Locate and identify every blood parasite.
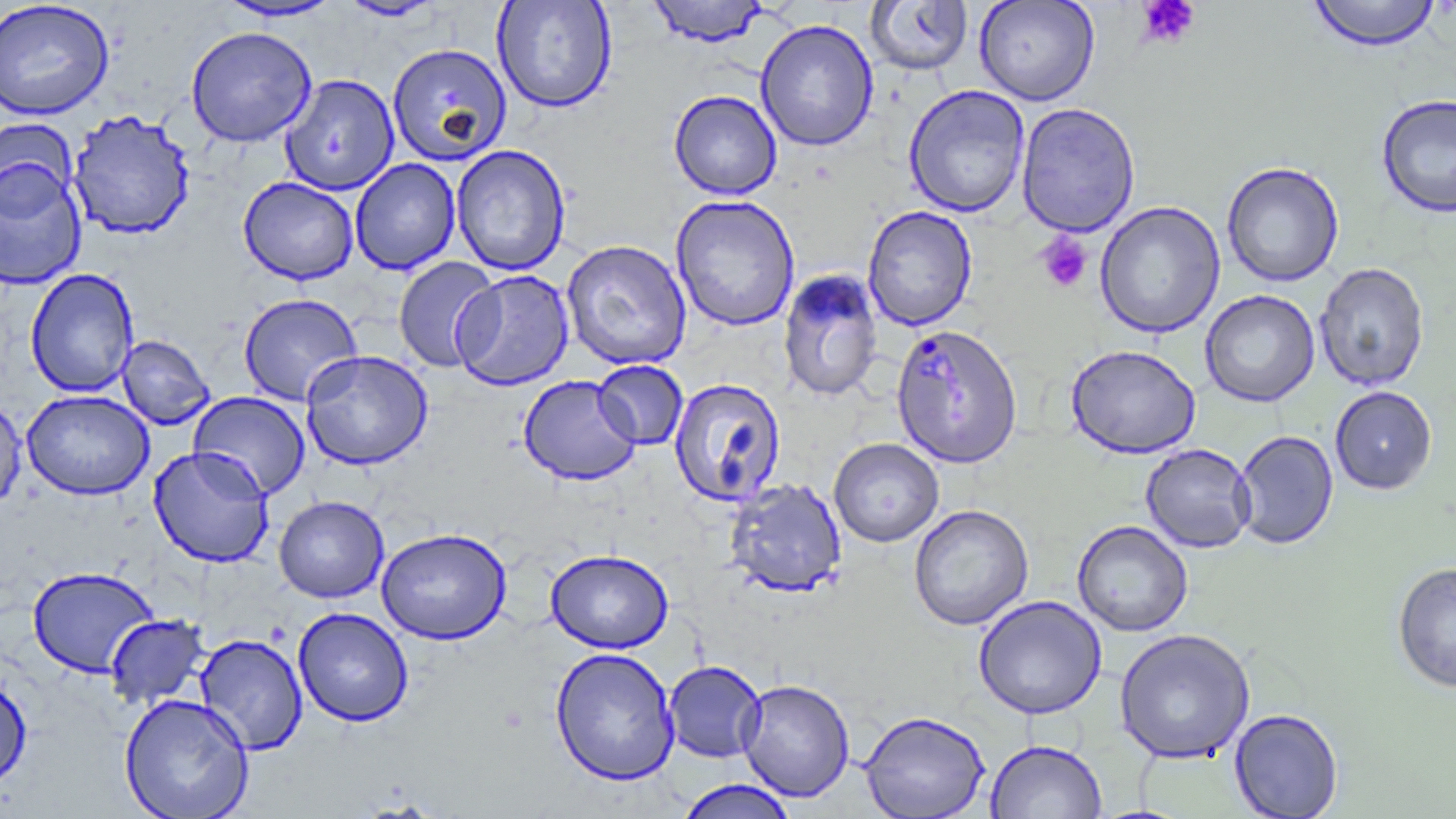

Approximate bounding boxes as (x1, y1, x2, y2) in pixels.
Plasmodium falciparum-infected red blood cells: (890, 324, 1023, 469).
No Plasmodium ovale, Plasmodium malariae, Plasmodium vivax, Babesia divergens, or Trypanosoma brucei observed.

Summary:
  - Uninfected red blood cell locations: (337, 0, 445, 22), (492, 0, 617, 114), (647, 0, 769, 47), (974, 0, 1100, 106), (1306, 0, 1442, 52), (0, 1, 115, 122), (216, 1, 345, 22), (864, 1, 973, 75), (755, 19, 878, 152), (186, 26, 316, 147), (387, 43, 511, 166), (280, 73, 400, 196), (903, 85, 1030, 217), (668, 90, 782, 200), (1376, 93, 1456, 219), (1016, 102, 1140, 237), (67, 109, 196, 241), (0, 118, 79, 218), (451, 144, 571, 276), (350, 158, 461, 275), (0, 159, 88, 291), (1221, 161, 1344, 288), (239, 176, 359, 285), (670, 195, 800, 332), (1095, 201, 1226, 338), (862, 205, 977, 332), (561, 239, 692, 370), (393, 257, 501, 373), (1314, 262, 1430, 391), (25, 267, 140, 398), (452, 269, 575, 391), (778, 269, 883, 402), (1200, 289, 1320, 407), (238, 293, 363, 406), (116, 335, 216, 430), (1065, 344, 1201, 459), (300, 350, 433, 471), (593, 360, 688, 450), (518, 375, 641, 486), (668, 377, 787, 508), (1330, 386, 1437, 494), (22, 390, 154, 499), (187, 391, 312, 500), (0, 396, 27, 513), (1232, 430, 1339, 549), (829, 438, 944, 547), (1140, 443, 1256, 553), (148, 445, 275, 568), (725, 478, 848, 598), (274, 495, 389, 603), (908, 504, 1034, 631), (1072, 520, 1193, 637), (376, 527, 512, 644), (545, 549, 674, 653), (1392, 561, 1456, 693), (26, 565, 159, 678), (973, 595, 1107, 719), (293, 607, 414, 727), (104, 613, 210, 711), (1114, 628, 1255, 764), (195, 633, 308, 755), (549, 646, 680, 786), (664, 660, 766, 763), (0, 673, 32, 791), (736, 679, 855, 802), (119, 693, 255, 819), (1229, 708, 1343, 818), (859, 709, 990, 818), (986, 740, 1107, 819), (674, 779, 799, 819)
  - Platelet locations: (1135, 0, 1202, 49), (1035, 232, 1093, 294)
  - Slide-level diagnosis: Plasmodium falciparum
  - Field of view: single
  - Magnification: 1000x
  - Image size: 1456×819 pixels
  - Modality: light microscopy
  - Stain: May-Grünwald-Giemsa
  - Preparation: thin blood film